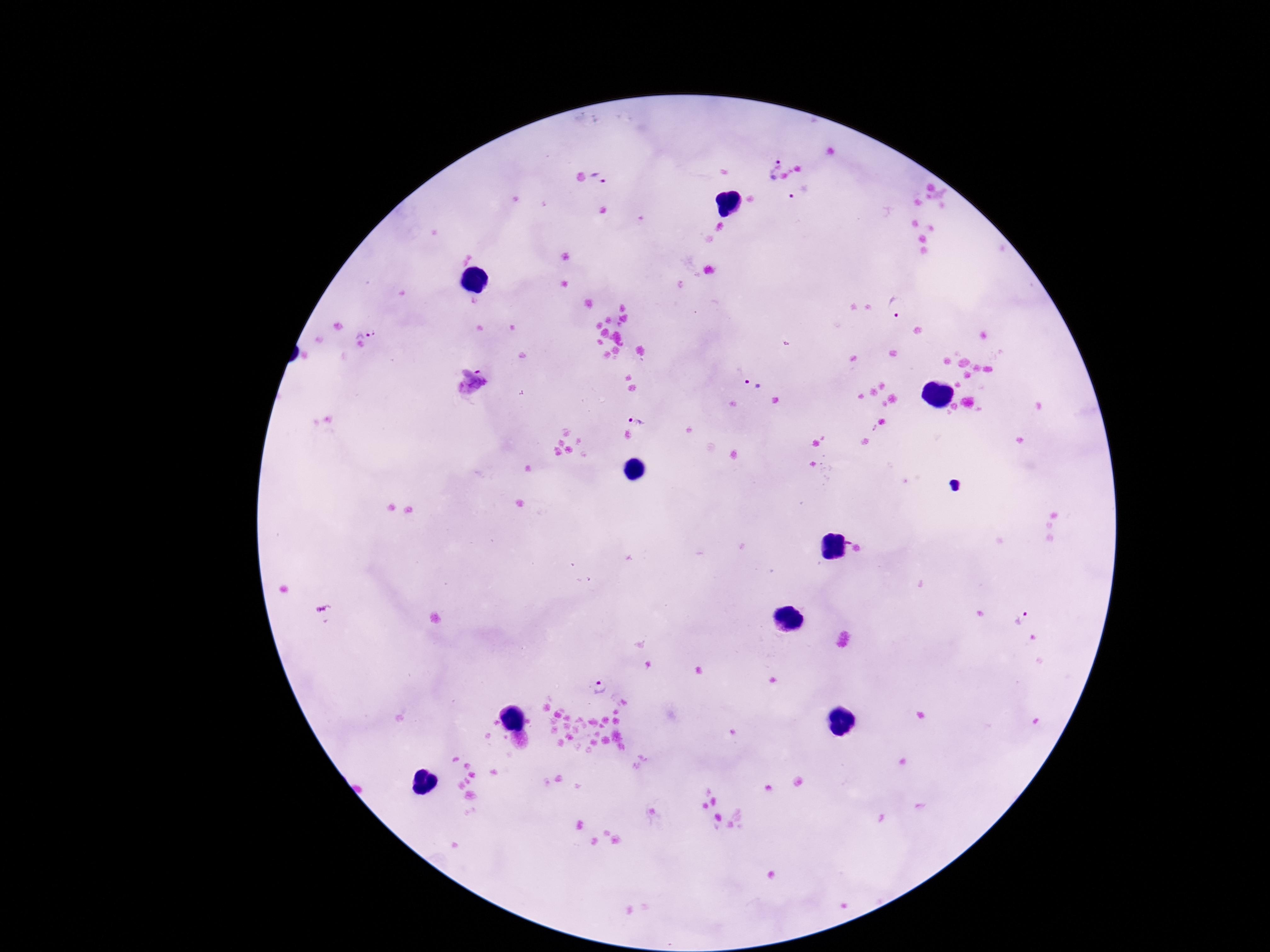

capture = smartphone camera through the microscope eyepiece
magnification = 100x
stain = Giemsa
Plasmodium parasite locations = approximate object centers, in pixels from the top-left corner: (x=773, y=167), (x=600, y=178), (x=800, y=192), (x=898, y=309), (x=365, y=325), (x=752, y=382), (x=637, y=416), (x=1022, y=620), (x=601, y=686)
image size = 1270×952 pixels
preparation = thick peripheral-blood smear
field of view = one from this slide
patient malaria status = positive